Assess this cell for malaria.
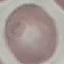
It is uninfected.

Summary:
  - Image type: cell patch, automatically extracted from a larger field of view and resized to 64 × 64 pixels
  - Capture: smartphone through the microscope eyepiece
  - Stain: Giemsa
  - Preparation: thin blood film